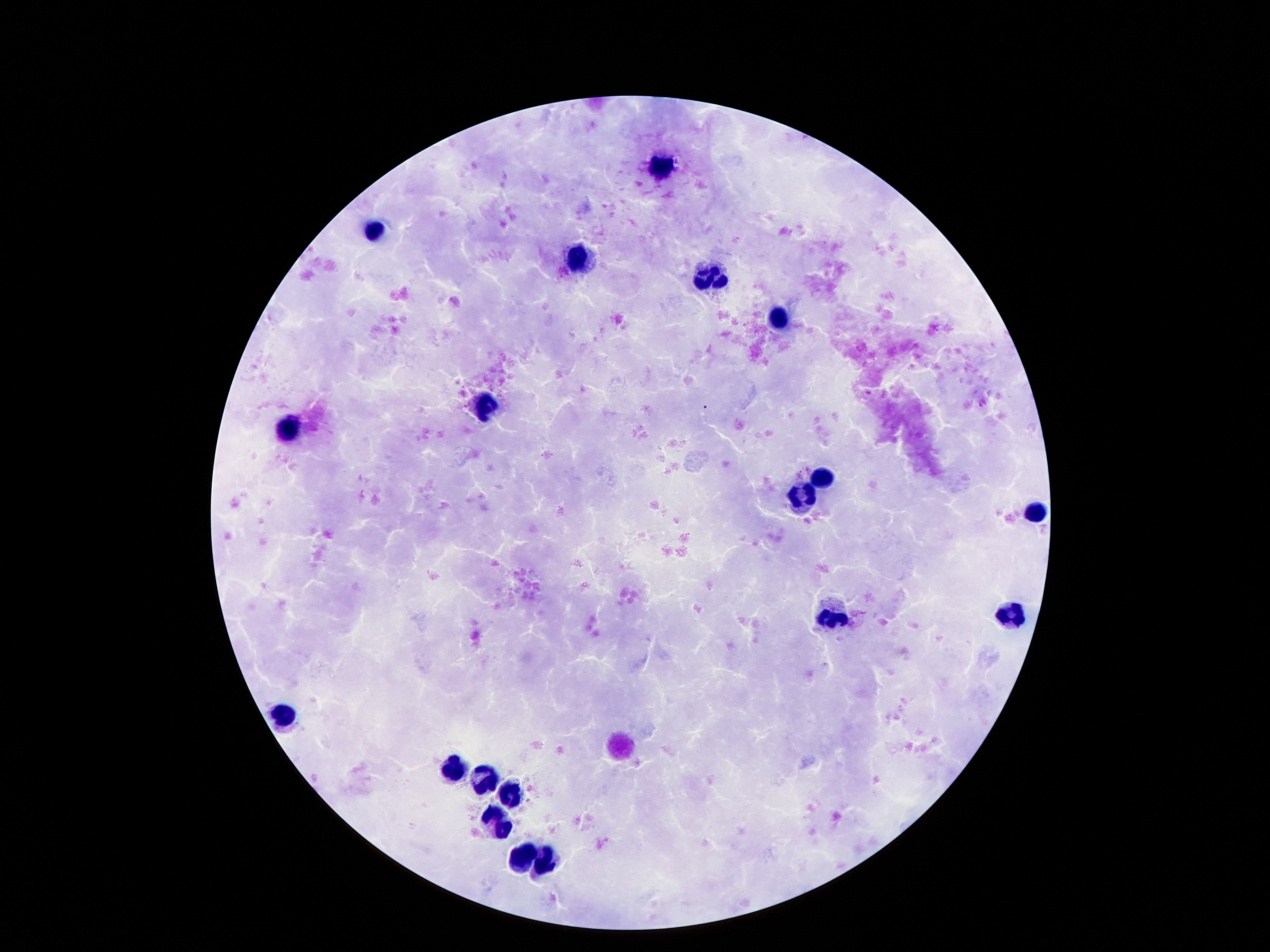

stain = Giemsa
leukocyte locations = approximate centers as {x, y} in pixels: {663, 169}, {372, 231}, {577, 261}, {708, 278}, {777, 317}, {480, 403}, {288, 431}, {823, 475}, {800, 499}, {1034, 516}, {833, 615}, {1013, 619}, {286, 714}, {450, 770}, {486, 778}, {507, 796}, {497, 826}, {521, 858}, {548, 862}
image size = 1270×952 pixels
capture = smartphone camera through the microscope eyepiece
preparation = thick blood film
magnification = 100x
field of view = one from this slide
patient malaria status = not infected